Outline each Plasmodium malariae-infected red blood cell.
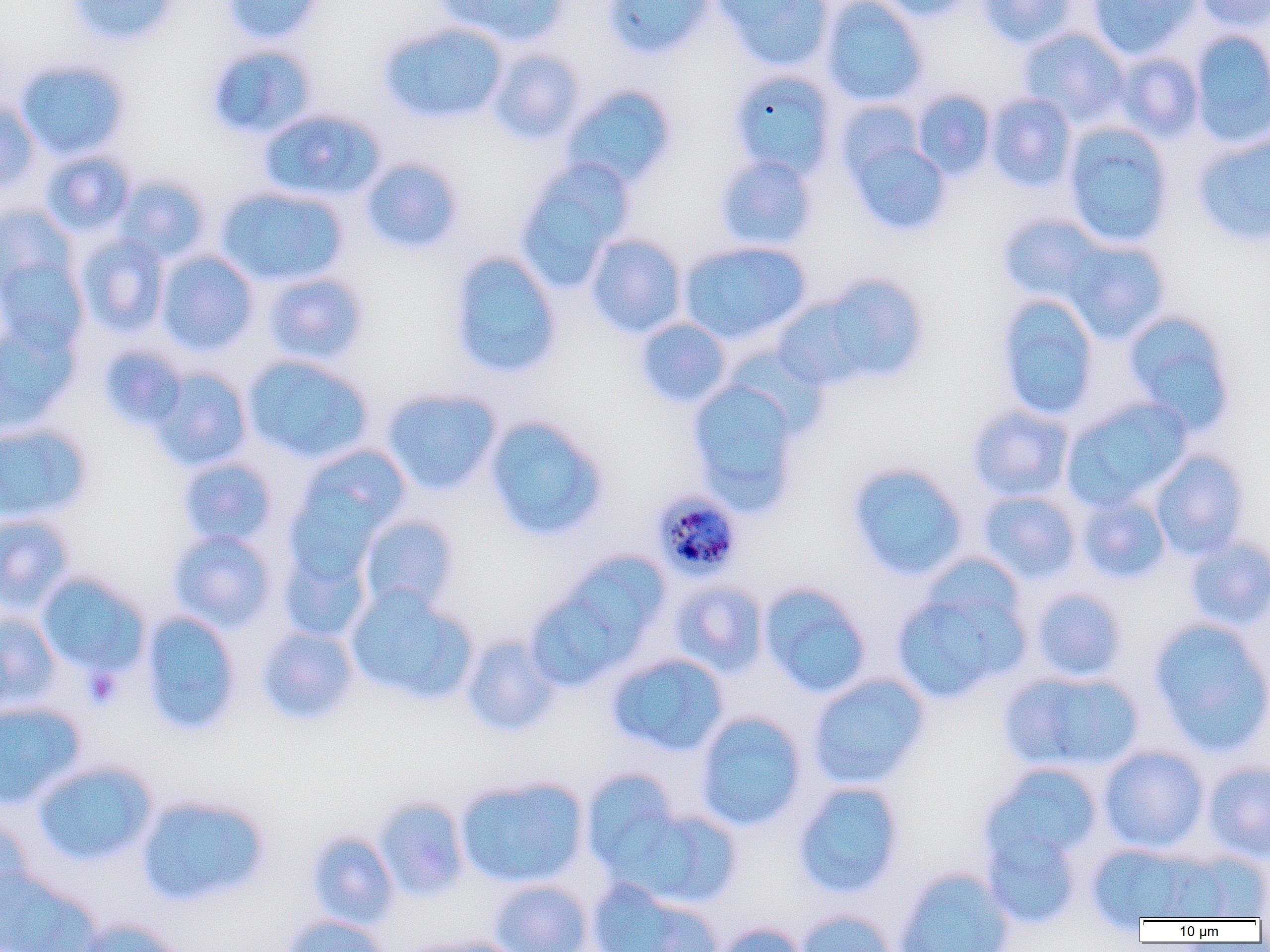
Approximate bounding boxes as (x1,y1)-(x2,y2) corner pairs in pixels.
Plasmodium malariae-infected red blood cells: (655,490)-(746,582).

slide-level diagnosis = Plasmodium malariae
platelet locations = approximate bounding boxes as (x1,y1)-(x2,y2) corner pairs in pixels: (82,666)-(123,708)
uninfected red blood cell locations = approximate bounding boxes as (x1,y1)-(x2,y2) corner pairs in pixels: (66,0)-(179,46), (221,0)-(326,45), (436,0)-(571,47), (602,0)-(715,60), (712,0)-(834,72), (820,0)-(929,107), (876,0)-(977,21), (976,0)-(1078,49), (1086,0)-(1201,60), (1192,0)-(1270,34), (378,21)-(509,126), (1017,27)-(1130,128), (1189,29)-(1270,148), (206,42)-(320,141), (487,47)-(587,146), (1113,52)-(1205,142), (15,58)-(132,161), (728,69)-(838,180), (560,84)-(678,190), (911,89)-(996,181), (985,92)-(1077,193), (0,97)-(41,193), (834,99)-(926,185), (258,108)-(387,204), (1063,122)-(1175,249), (843,131)-(951,236), (1192,132)-(1270,247), (39,149)-(136,237), (714,154)-(818,252), (359,157)-(464,255), (514,157)-(635,291), (113,174)-(211,265), (215,185)-(349,287), (0,201)-(79,298), (996,212)-(1110,306), (75,233)-(170,337), (584,233)-(688,338), (1061,237)-(1172,345), (677,240)-(812,346), (155,250)-(260,356), (447,250)-(563,380), (0,254)-(90,355), (261,272)-(370,366), (808,273)-(930,386), (768,290)-(885,392), (994,293)-(1100,422), (1121,309)-(1238,436), (0,317)-(80,435), (634,317)-(733,409), (97,344)-(189,431), (242,355)-(375,464), (147,366)-(254,472), (686,378)-(803,515), (380,387)-(503,496), (1061,397)-(1192,511), (966,405)-(1075,502), (483,415)-(608,542), (0,422)-(93,524), (293,444)-(413,547), (1149,448)-(1250,560), (176,456)-(279,548), (846,461)-(970,582), (976,490)-(1082,584), (1077,493)-(1171,584), (0,512)-(76,614), (358,515)-(460,612), (167,529)-(277,633), (1183,535)-(1270,631), (277,541)-(374,644), (559,550)-(672,653), (35,571)-(151,677), (890,576)-(1030,704), (668,579)-(769,677), (758,582)-(872,699), (344,585)-(479,706), (1030,586)-(1128,683), (524,589)-(634,692), (0,609)-(62,712), (139,609)-(242,737), (1147,617)-(1270,755), (255,626)-(360,725), (461,633)-(563,737), (607,653)-(730,757), (999,669)-(1145,775), (807,672)-(931,789), (0,700)-(87,809), (694,710)-(809,832), (1097,744)-(1210,855), (32,759)-(159,868), (1203,759)-(1270,863), (980,764)-(1105,871), (580,769)-(684,875), (454,775)-(589,889), (792,780)-(906,899), (136,793)-(271,908), (373,795)-(470,901), (617,806)-(743,910), (0,817)-(35,914), (981,826)-(1083,929), (306,830)-(400,930), (1086,843)-(1209,925), (1156,847)-(1269,920), (894,867)-(1016,952), (487,879)-(594,952), (587,880)-(722,952), (795,908)-(898,952), (282,914)-(390,952), (74,917)-(186,952), (710,920)-(811,952), (400,935)-(528,952)
preparation = thin blood smear
modality = light microscopy
field of view = one of a larger specimen
image size = 1270×952 pixels
magnification = 1000x